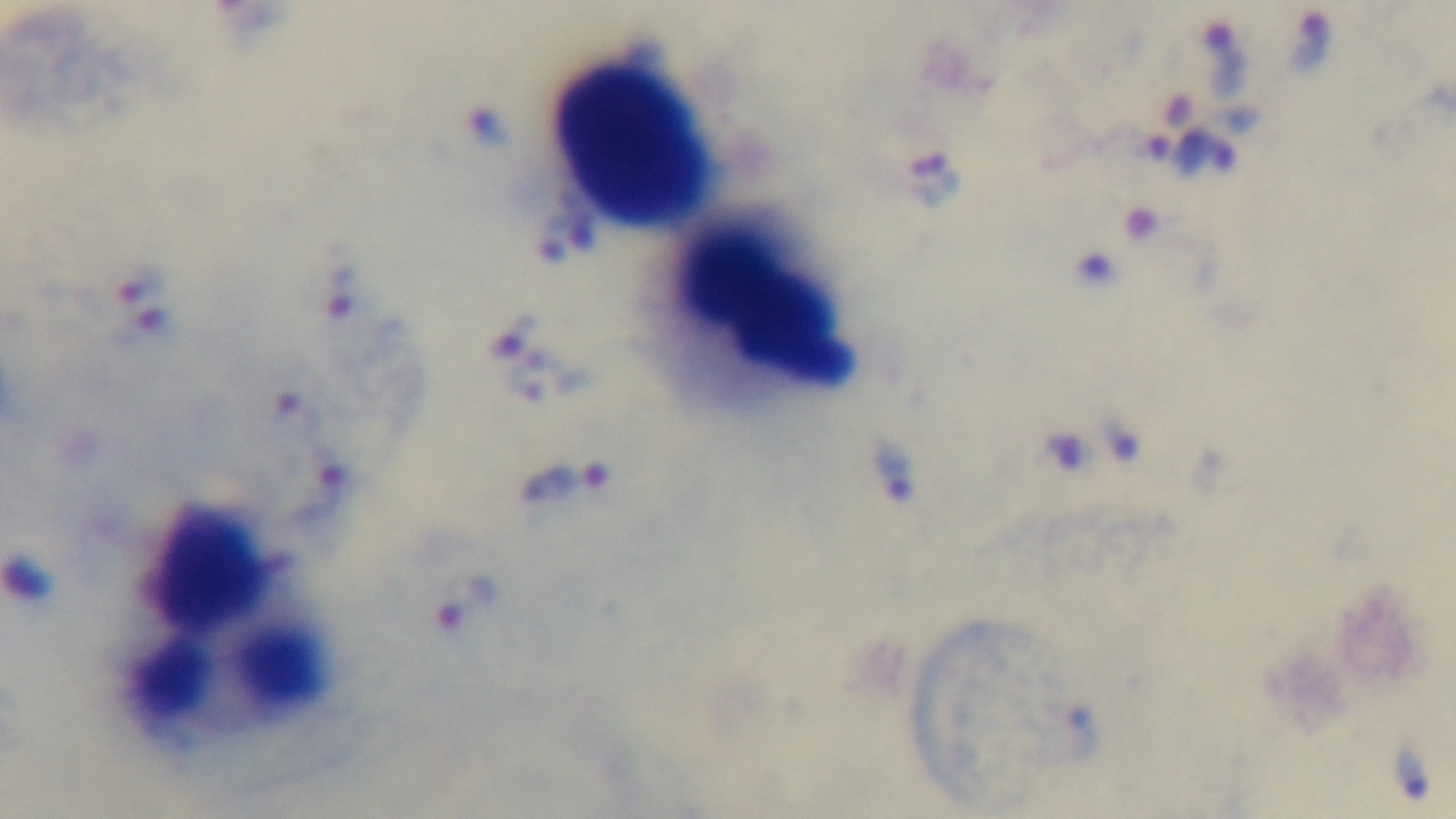

capture: mounted 4K digital camera
field_of_view: one from the slide
malaria_status: infected
preparation: thick blood film
stain: Giemsa
modality: light microscopy
objective: 100x oil immersion